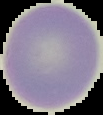

preparation = thin blood film
malaria status = uninfected
image size = 103×115 pixels
image type = segmented cell region with the area outside set to black